Locate every Plasmodium falciparum-infected red blood cell.
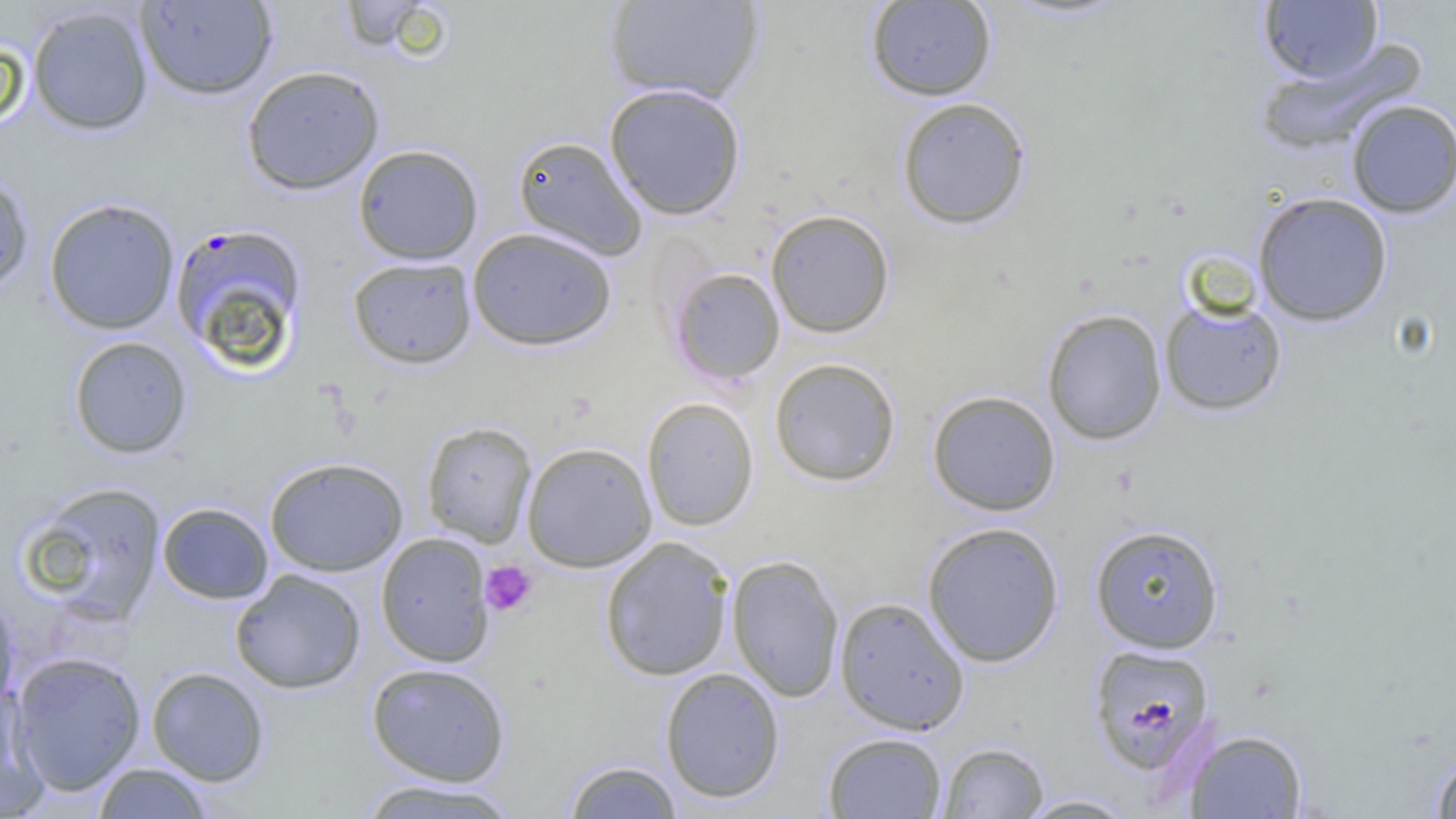
Approximate bounding boxes as (x1,y1)-(x2,y2) corner pairs in pixels.
Plasmodium falciparum-infected red blood cells: (169,222)-(309,369), (1088,642)-(1217,776).

Uninfected red blood cell locations: (335,0)-(446,54), (603,0)-(764,106), (865,0)-(997,101), (135,1)-(277,100), (1258,1)-(1384,84), (27,5)-(154,135), (1259,40)-(1425,154), (241,65)-(385,195), (604,82)-(747,220), (896,97)-(1032,230), (1345,99)-(1456,218), (512,135)-(649,261), (353,144)-(484,265), (0,169)-(35,295), (1251,191)-(1394,326), (43,197)-(181,335), (765,209)-(896,338), (467,226)-(618,351), (347,256)-(477,369), (667,267)-(786,386), (1159,296)-(1288,416), (1042,308)-(1167,445), (68,336)-(192,459), (768,357)-(902,486), (926,390)-(1061,516), (642,397)-(759,532), (421,421)-(537,548), (521,441)-(658,572), (265,456)-(408,576), (18,481)-(168,625), (157,502)-(273,604), (921,521)-(1065,668), (1089,524)-(1225,653), (376,532)-(495,667), (599,536)-(735,682), (726,555)-(844,702), (230,569)-(366,694), (0,588)-(20,716), (834,597)-(970,735), (10,651)-(146,795), (366,662)-(511,786), (146,666)-(270,786), (659,667)-(786,804), (0,684)-(50,817), (1183,728)-(1309,818), (822,732)-(947,818), (937,741)-(1050,818), (1430,749)-(1456,818), (561,759)-(685,818), (91,762)-(215,818), (356,778)-(521,819), (1015,793)-(1142,818). Platelet locations: (480,560)-(538,616). Slide-level diagnosis: Plasmodium falciparum. Light microscopy. Image is 1456×819 pixels. Thin blood smear. 1000x magnification. One field of a larger specimen.